Classify this cell by malaria status.
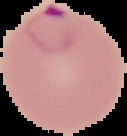

It is parasitized.

The area outside the segmented cell region is set to black. Image is 127×136 pixels. From a thin blood film.